Assess the morphology of the erythrocytes.
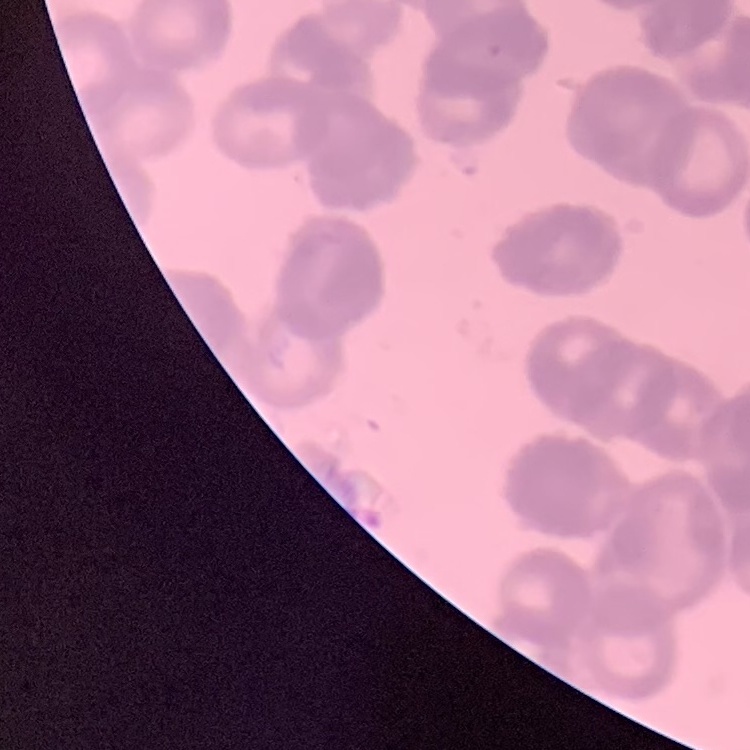
Rouleaux formation.

Summary:
  - Image type: one tile cut from a larger photomicrograph
  - Preparation: thin blood film
  - Stain: Field's or Giemsa